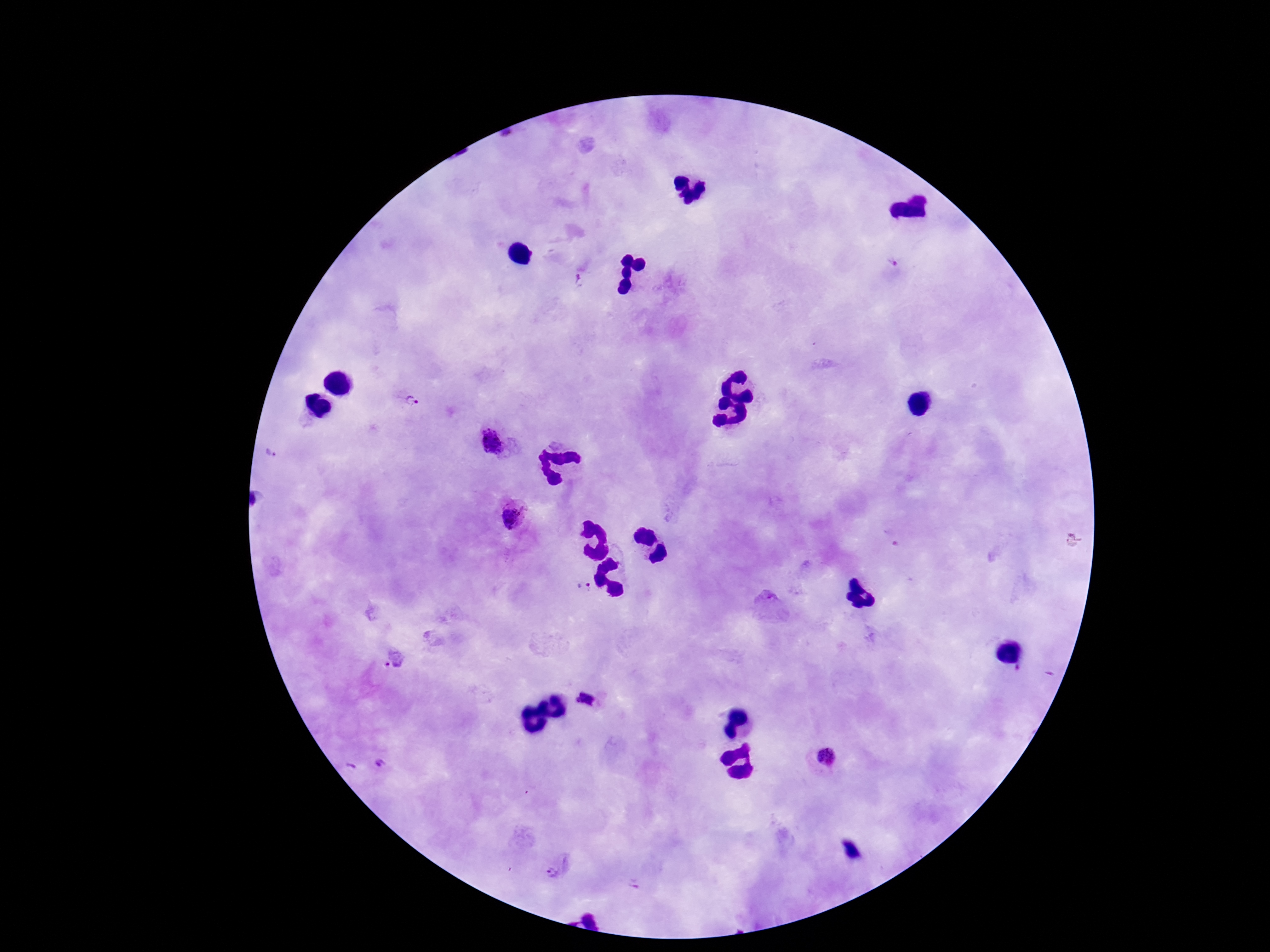

{
  "field_of_view": "one from this slide",
  "patient_malaria_status": "positive",
  "plasmodium_parasite_locations": "approximate centers as [x, y] in pixels: [892, 264], [580, 282], [413, 402], [493, 445], [270, 454], [511, 519], [586, 589], [393, 660], [592, 698], [823, 759], [381, 762], [351, 768], [552, 873]",
  "preparation": "thick blood film",
  "magnification": "100x",
  "image_size": "1270×952 pixels",
  "capture": "smartphone camera through the microscope eyepiece",
  "stain": "Giemsa"
}